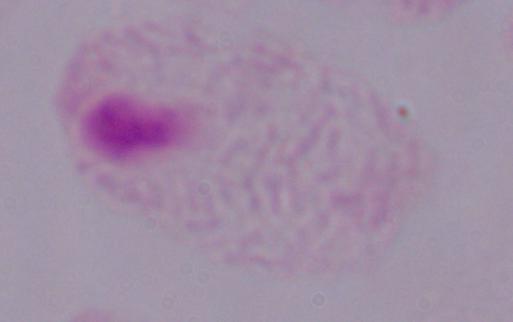
modality = photomicrograph
identification = trichomonad
magnification = 1000x